Comment on the morphology of the erythrocytes.
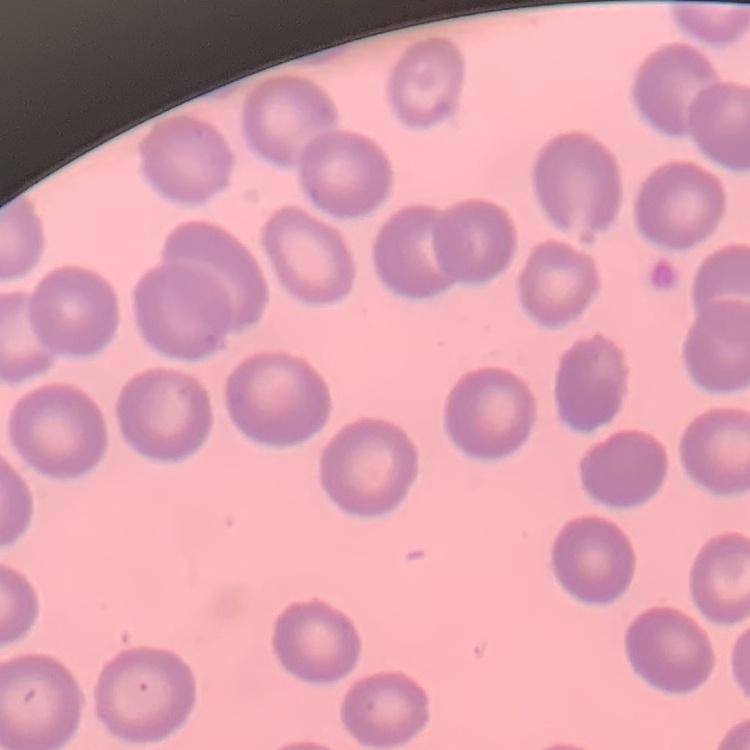

No rouleaux formation.

Thin peripheral smear. Field's or Giemsa stain. One tile cut from a larger photomicrograph.